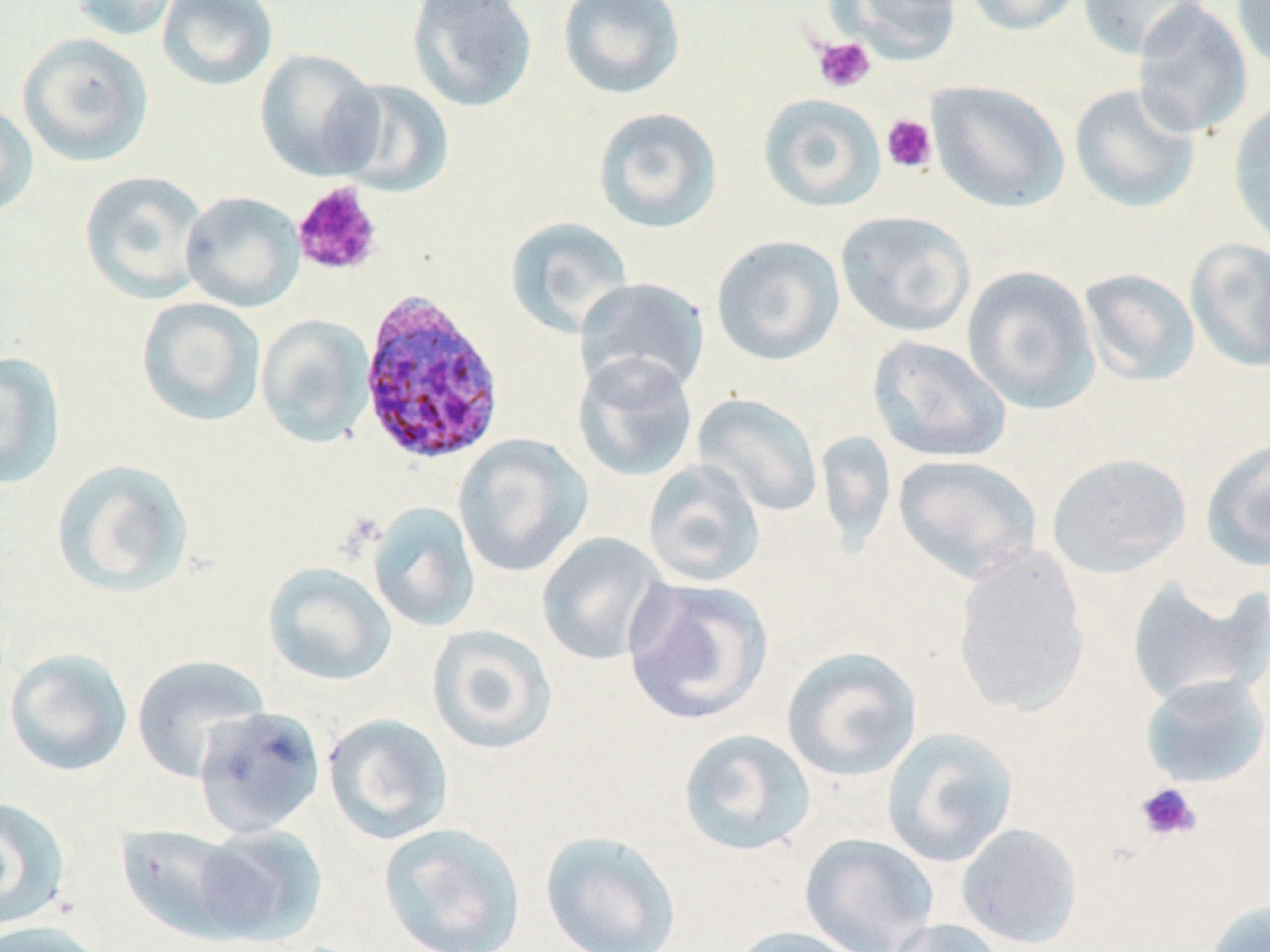
{
  "slide_level_diagnosis": "Plasmodium ovale",
  "uninfected_red_blood_cell_locations": "approximate bounding boxes as (x1, y1, x2, y2) in pixels: (69, 0, 183, 40), (157, 0, 278, 92), (406, 0, 538, 113), (557, 0, 686, 101), (835, 0, 963, 63), (964, 0, 1085, 36), (1077, 0, 1210, 60), (1131, 0, 1253, 139), (1232, 0, 1270, 74), (17, 32, 154, 167), (255, 48, 384, 181), (330, 79, 454, 197), (927, 81, 1069, 213), (1068, 83, 1201, 213), (758, 93, 886, 212), (1228, 97, 1270, 247), (0, 100, 39, 219), (592, 106, 723, 234), (79, 170, 211, 304), (180, 191, 305, 312), (836, 210, 977, 338), (505, 216, 635, 338), (711, 235, 845, 366), (1185, 237, 1270, 372), (961, 264, 1100, 414), (1078, 268, 1200, 387), (574, 277, 710, 398), (136, 297, 267, 427), (256, 314, 375, 449), (867, 335, 1012, 464), (0, 351, 66, 490), (572, 351, 699, 482), (693, 393, 823, 518), (815, 430, 896, 557), (453, 434, 592, 577), (1201, 437, 1270, 572), (1047, 452, 1191, 578), (893, 454, 1042, 582), (50, 458, 196, 598), (643, 459, 765, 588), (367, 501, 481, 632), (536, 532, 672, 666), (951, 545, 1090, 717), (262, 561, 397, 687), (1126, 574, 1269, 707), (622, 577, 773, 726), (426, 624, 559, 755), (781, 647, 923, 782), (4, 648, 133, 777), (131, 654, 271, 781), (1139, 673, 1270, 789), (194, 706, 326, 838), (323, 713, 454, 845), (882, 727, 1019, 867), (677, 728, 816, 857), (0, 796, 71, 932), (378, 822, 527, 952), (957, 822, 1082, 949), (116, 823, 248, 942), (192, 824, 327, 946), (540, 830, 682, 952), (799, 833, 938, 952), (1202, 898, 1270, 952), (885, 918, 1009, 952), (0, 920, 108, 952), (724, 925, 873, 952)",
  "field_of_view": "one of a larger specimen",
  "magnification": "1000x",
  "preparation": "thin blood film",
  "platelet_locations": "approximate bounding boxes as (x1, y1, x2, y2) in pixels: (812, 35, 875, 93), (881, 114, 937, 173), (292, 182, 383, 277), (1135, 782, 1201, 841)",
  "stain": "May-Grünwald-Giemsa",
  "modality": "optical microscopy",
  "image_size": "1270×952 pixels",
  "plasmodium_ovale_infected_red_blood_cell_locations": "approximate bounding boxes as (x1, y1, x2, y2) in pixels: (357, 287, 506, 466)"
}